Give the preparation type.
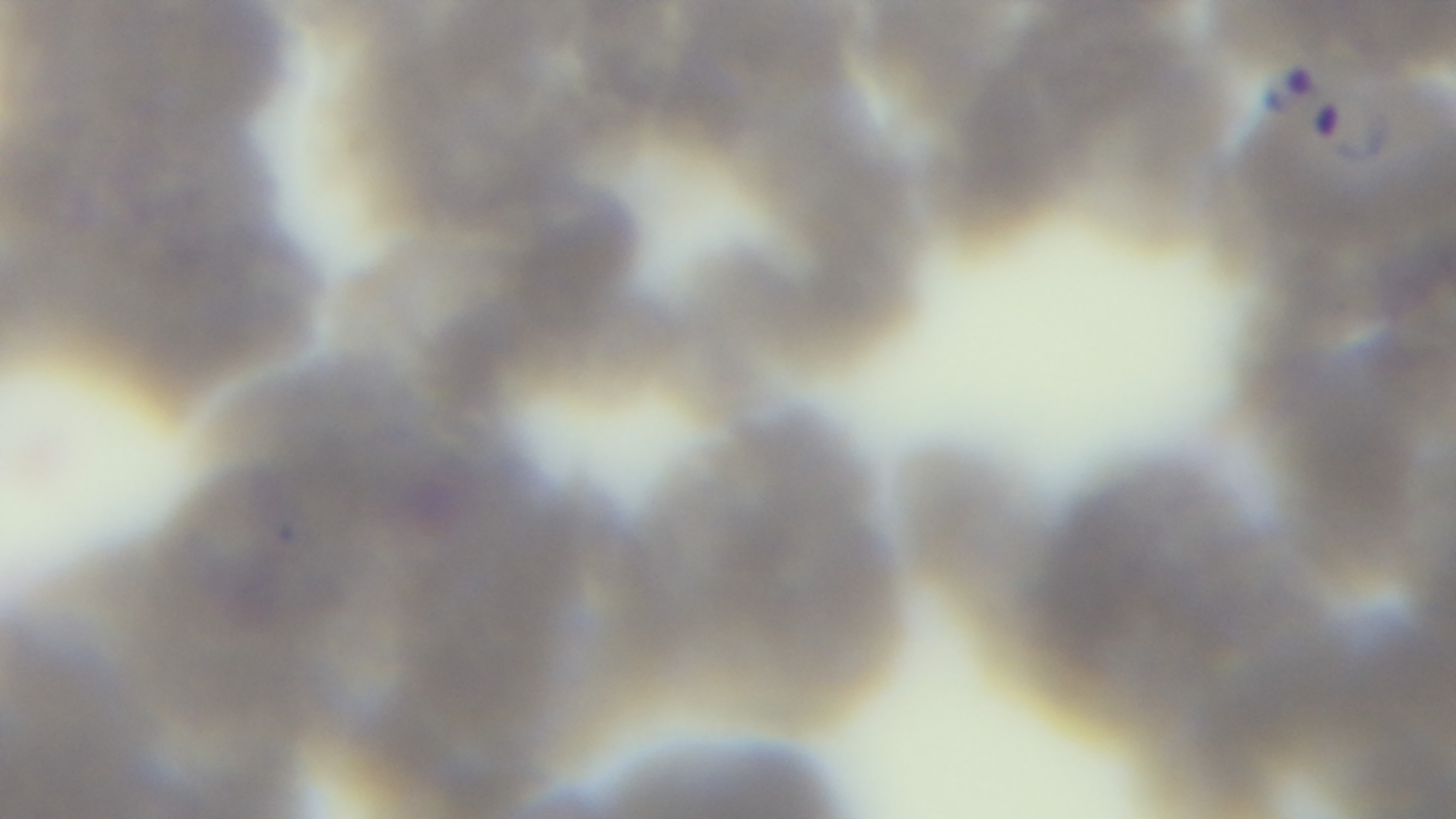

A thin smear.

malaria status = positive
modality = light microscopy
field of view = one from the slide
stain = Giemsa
objective = 100x oil immersion
capture = mounted 4K digital camera